State the blood parasite species.
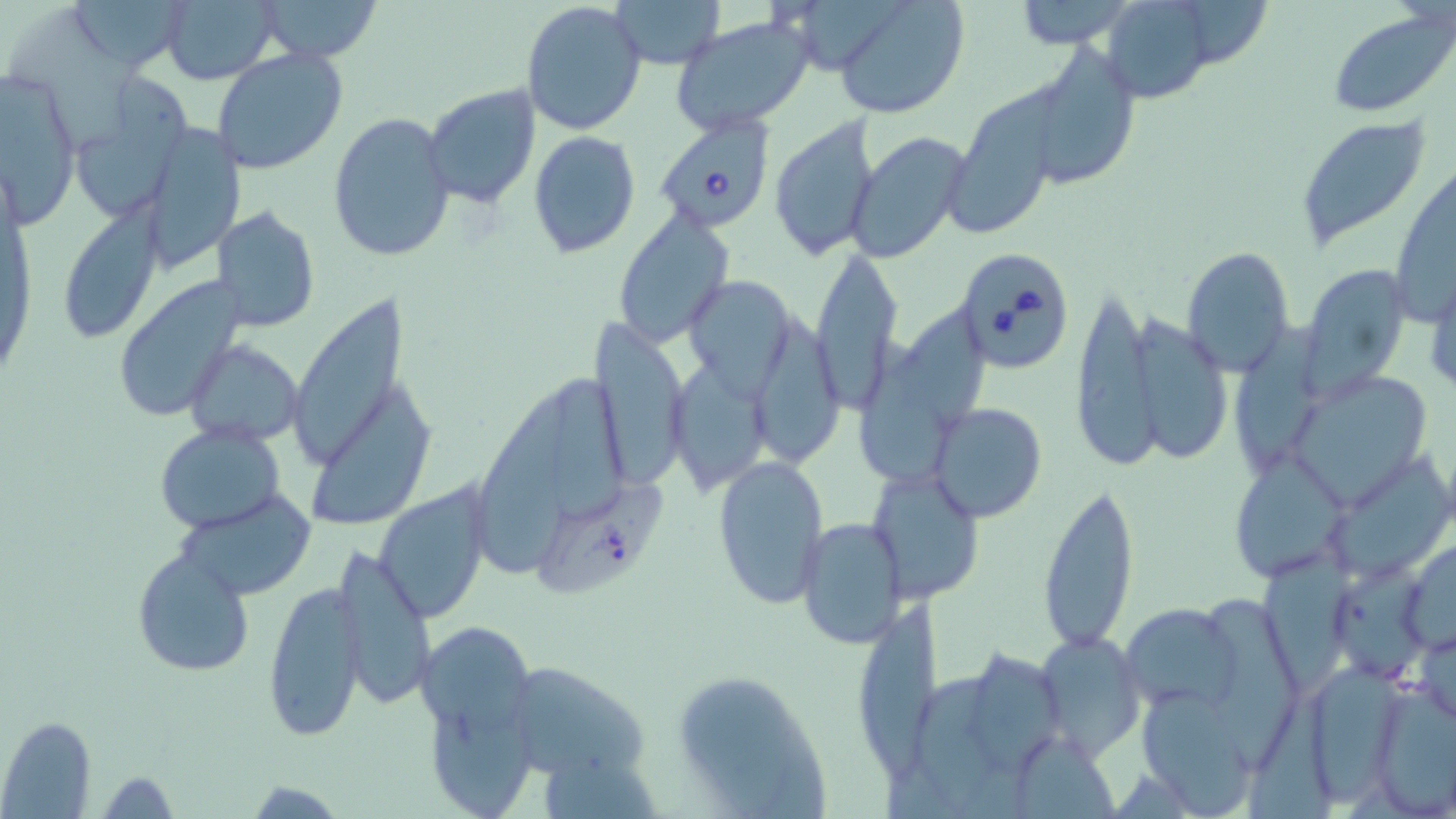
Babesia divergens.

Approximate bounding boxes as named x1/y1/x2/y2 corners in pixels. Babesia divergens-infected red blood cell locations: (x1=650, y1=114, x2=775, y2=235), (x1=952, y1=246, x2=1076, y2=373). Uninfected red blood cell locations: (x1=70, y1=0, x2=188, y2=67), (x1=159, y1=0, x2=282, y2=86), (x1=257, y1=0, x2=384, y2=64), (x1=612, y1=0, x2=723, y2=69), (x1=830, y1=0, x2=969, y2=120), (x1=1005, y1=0, x2=1143, y2=47), (x1=1097, y1=0, x2=1223, y2=103), (x1=520, y1=1, x2=647, y2=137), (x1=1328, y1=8, x2=1456, y2=116), (x1=668, y1=14, x2=816, y2=136), (x1=1020, y1=44, x2=1141, y2=191), (x1=212, y1=48, x2=347, y2=175), (x1=0, y1=69, x2=81, y2=224), (x1=77, y1=75, x2=195, y2=225), (x1=423, y1=83, x2=542, y2=208), (x1=942, y1=104, x2=1059, y2=236), (x1=328, y1=110, x2=456, y2=262), (x1=770, y1=115, x2=883, y2=263), (x1=1294, y1=115, x2=1433, y2=253), (x1=140, y1=125, x2=245, y2=271), (x1=527, y1=131, x2=641, y2=258), (x1=847, y1=131, x2=973, y2=265), (x1=67, y1=196, x2=171, y2=336), (x1=213, y1=205, x2=320, y2=332), (x1=612, y1=208, x2=735, y2=346), (x1=809, y1=247, x2=902, y2=409), (x1=1180, y1=247, x2=1297, y2=376), (x1=1300, y1=263, x2=1415, y2=394), (x1=1425, y1=267, x2=1456, y2=402), (x1=683, y1=273, x2=798, y2=392), (x1=114, y1=279, x2=245, y2=424), (x1=1070, y1=287, x2=1158, y2=472), (x1=289, y1=292, x2=423, y2=467), (x1=1129, y1=306, x2=1232, y2=465), (x1=771, y1=313, x2=843, y2=466), (x1=906, y1=315, x2=992, y2=433), (x1=1232, y1=319, x2=1326, y2=468), (x1=589, y1=320, x2=691, y2=490), (x1=186, y1=340, x2=305, y2=444), (x1=864, y1=348, x2=950, y2=479), (x1=667, y1=358, x2=775, y2=496), (x1=545, y1=366, x2=635, y2=517), (x1=1286, y1=370, x2=1435, y2=506), (x1=312, y1=384, x2=440, y2=526), (x1=478, y1=393, x2=578, y2=576), (x1=929, y1=401, x2=1048, y2=523), (x1=155, y1=424, x2=284, y2=533), (x1=713, y1=453, x2=829, y2=609), (x1=1237, y1=454, x2=1352, y2=577), (x1=865, y1=467, x2=988, y2=607), (x1=1038, y1=479, x2=1140, y2=653), (x1=374, y1=486, x2=491, y2=623), (x1=174, y1=492, x2=314, y2=602), (x1=816, y1=492, x2=960, y2=628), (x1=796, y1=518, x2=907, y2=647), (x1=1258, y1=536, x2=1349, y2=690), (x1=1398, y1=540, x2=1456, y2=655), (x1=327, y1=545, x2=435, y2=712), (x1=132, y1=547, x2=254, y2=678), (x1=263, y1=580, x2=367, y2=740), (x1=1119, y1=602, x2=1243, y2=715), (x1=855, y1=604, x2=960, y2=786), (x1=418, y1=618, x2=545, y2=805), (x1=1035, y1=631, x2=1146, y2=758), (x1=975, y1=645, x2=1064, y2=770), (x1=501, y1=659, x2=651, y2=785), (x1=912, y1=667, x2=996, y2=809), (x1=669, y1=669, x2=828, y2=813), (x1=1365, y1=680, x2=1456, y2=814), (x1=1140, y1=686, x2=1256, y2=815), (x1=1246, y1=687, x2=1337, y2=819), (x1=1, y1=717, x2=95, y2=817). Single field of view. May-Grünwald-Giemsa-stained preparation. 1000x magnification. Image is 1456×819 pixels. Thin blood smear. Optical microscopy.